Assess the morphology of the red blood cells.
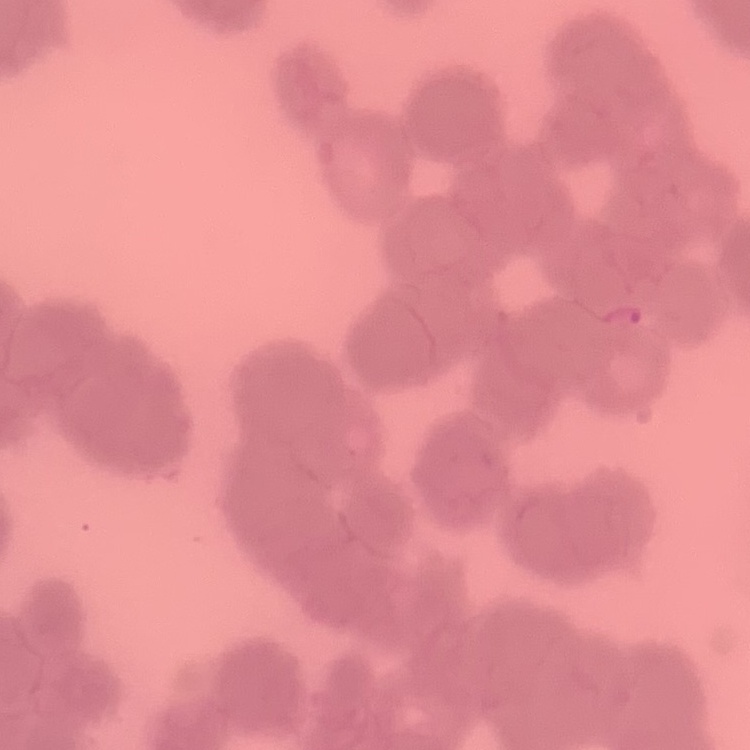
They show rouleaux formation.

Thin blood film. Square crop of a larger photomicrograph. Field's or Giemsa stain.